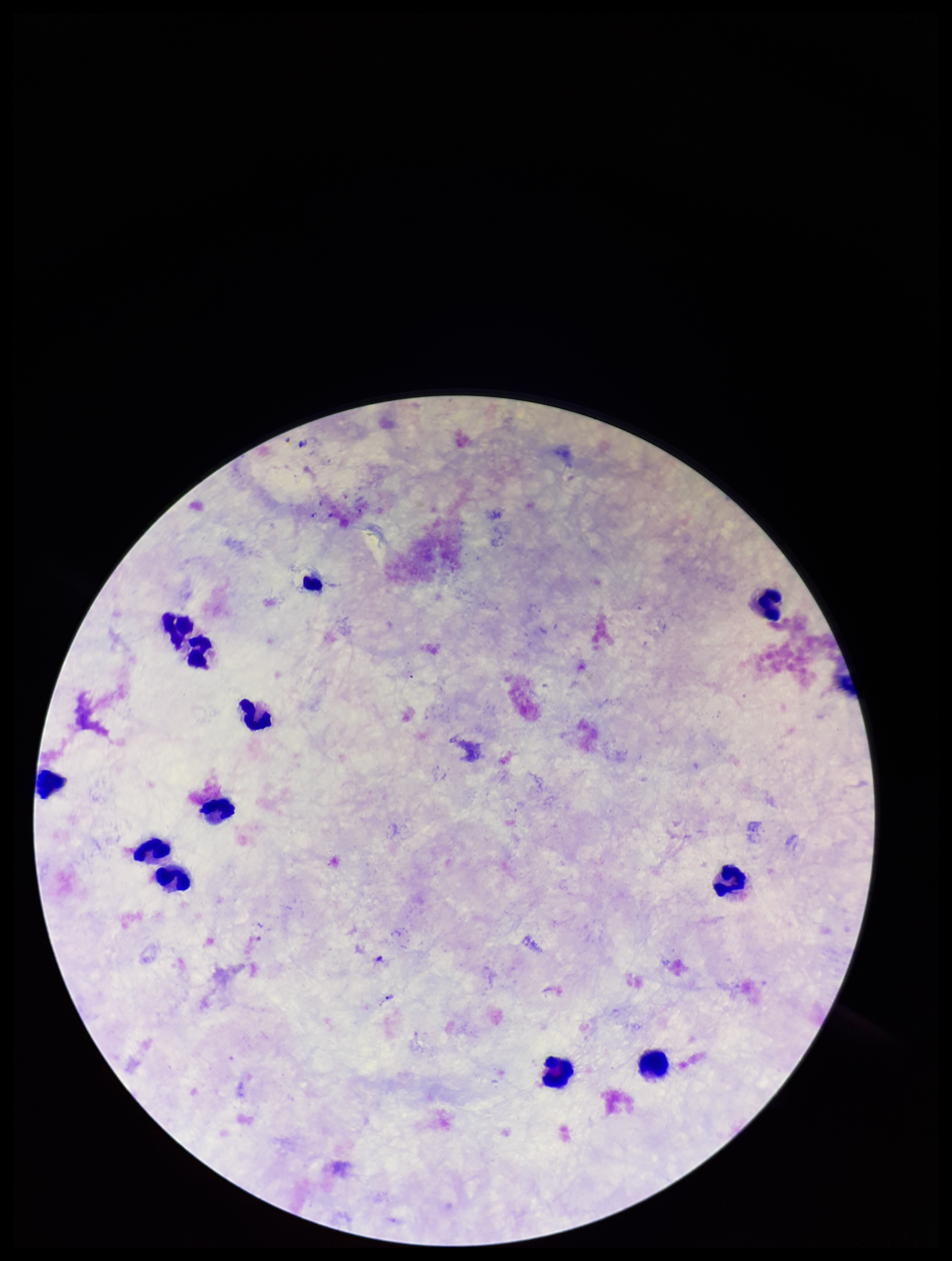
parasite count = 0
preparation = thick
capture = smartphone photograph through the microscope eyepiece
field of view = one from this slide
stain = Giemsa
patient malaria status = negative
Plasmodium parasites = none seen
image size = 952×1261 pixels
leukocyte count = 11